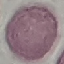

Malaria status: uninfected. Photographed with a smartphone camera at the microscope eyepiece. Cell patch, automatically extracted from a larger field of view and resized to 64 × 64 pixels. Giemsa stain. Thin smear of blood.